Name the parasite shown.
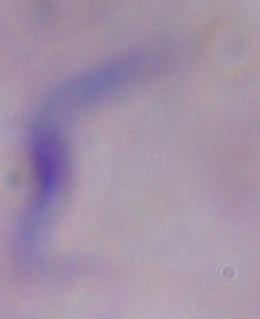

This is a trypanosome.

Micrograph. Captured at 1000x magnification.